Point out each Plasmodium parasite.
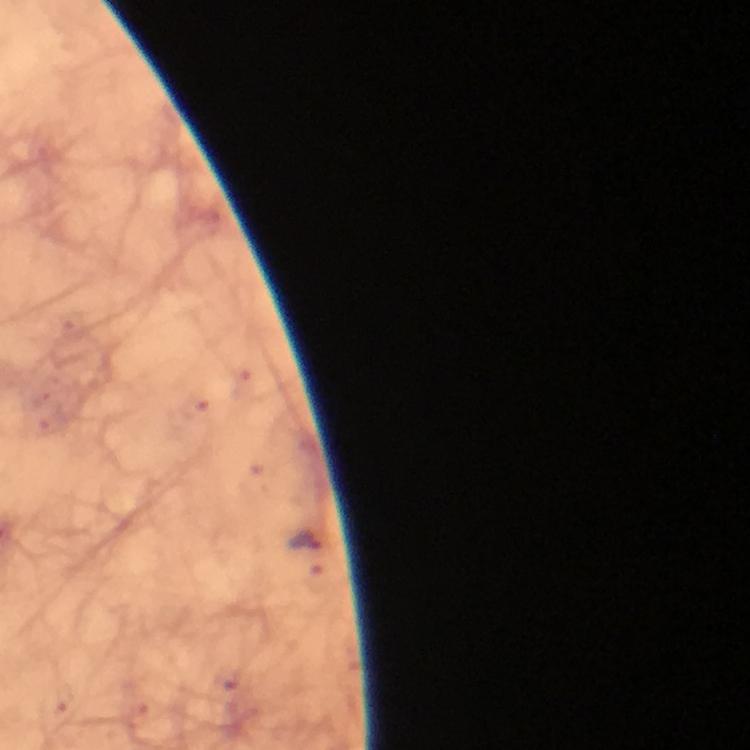

Approximate object centers, in pixels from the top-left corner.
Plasmodium parasites: (x=303, y=540).

Immersion oil was used. From a malaria diagnostic workup. Image is 750×750 pixels. Cropped region of a single field of view. 100x magnification. Giemsa-stained preparation. Thick blood smear. Photographed through the microscope with a smartphone camera.